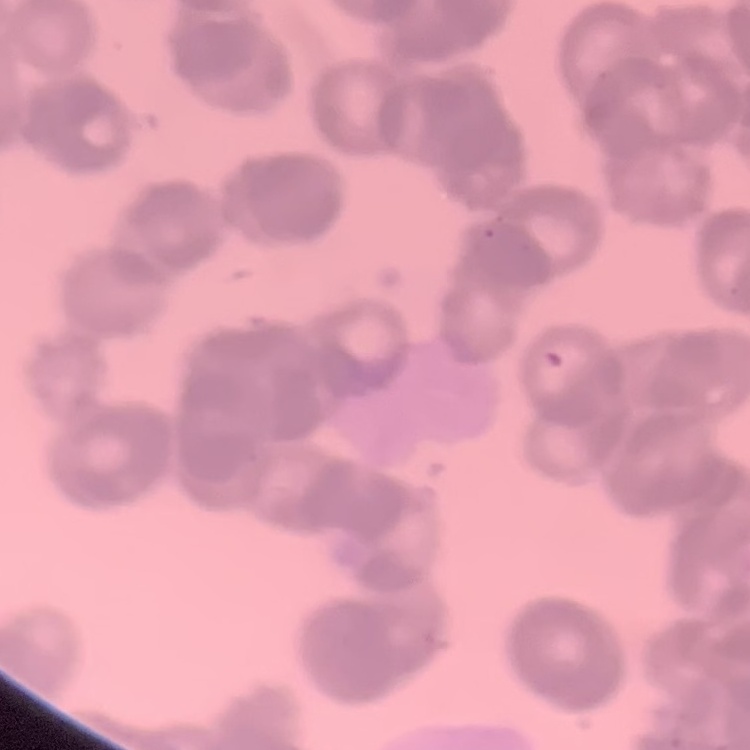 The red blood cells exhibit rouleaux formation. One tile cut from a larger photomicrograph. Thin blood film. Field's or Giemsa stain.